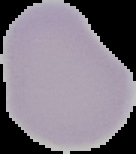
Malaria status: uninfected. Segmented cell region on a black background. Image is 136×154 pixels. From a thin blood smear.